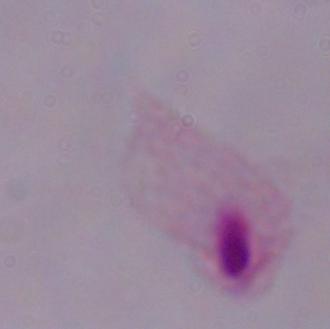
modality = micrograph
identification = trichomonad
magnification = 1000x